Outline each blood parasite and name the species.
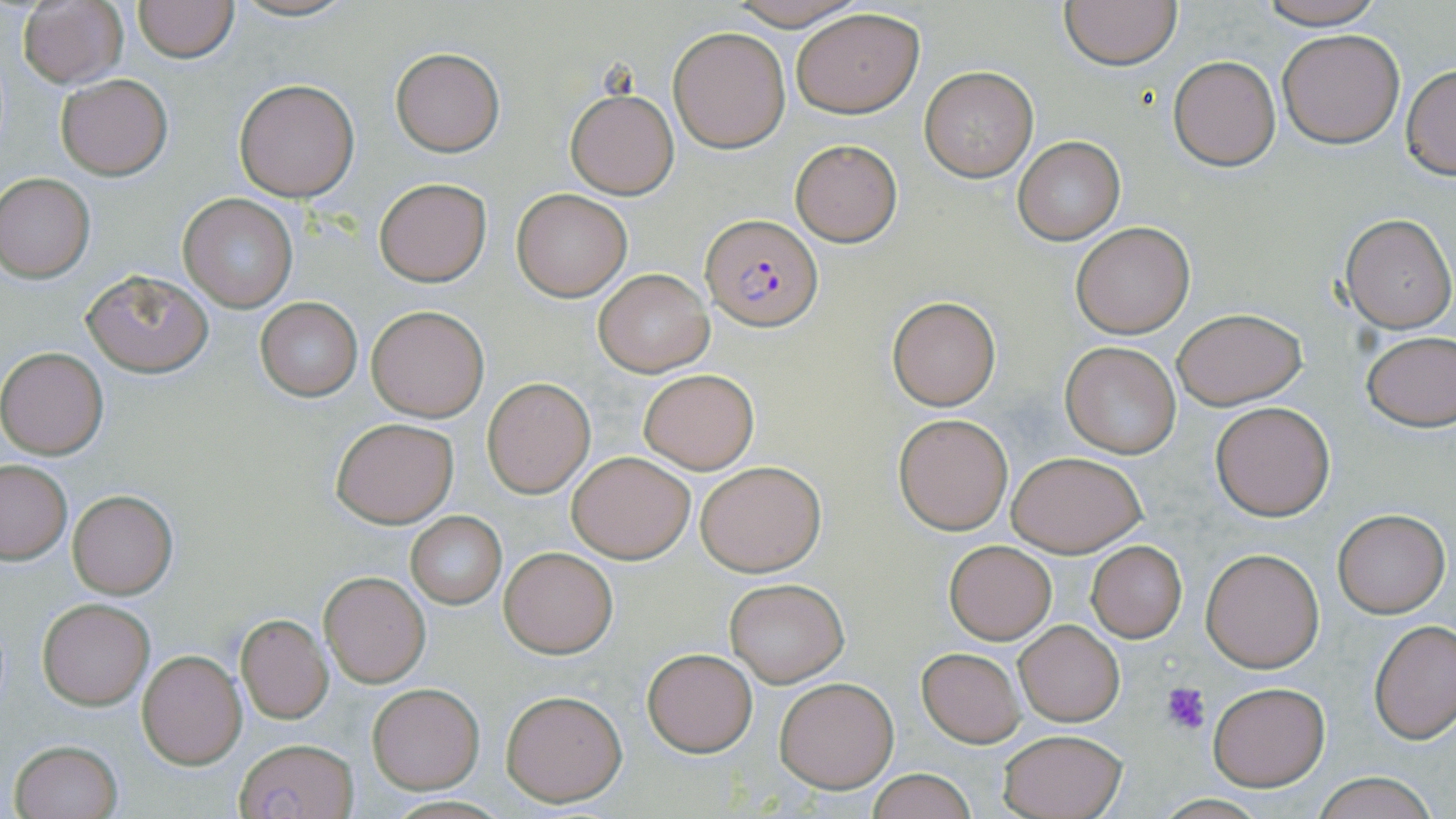

Approximate bounding boxes as [x1, y1, x2, y2] in pixels.
Plasmodium falciparum-infected red blood cells: [702, 214, 824, 333].
No Plasmodium ovale, Plasmodium malariae, Plasmodium vivax, Babesia divergens, or Trypanosoma brucei observed.

Platelet locations: [1162, 681, 1211, 734]. Uninfected red blood cell locations: [133, 0, 239, 62], [227, 0, 357, 22], [723, 0, 873, 29], [1253, 0, 1389, 29], [18, 1, 127, 88], [1060, 1, 1182, 70], [792, 7, 925, 119], [668, 25, 790, 152], [1277, 27, 1406, 148], [390, 47, 504, 155], [1168, 56, 1280, 170], [1401, 63, 1456, 179], [920, 65, 1038, 182], [55, 72, 174, 181], [232, 79, 360, 202], [565, 89, 679, 198], [1013, 137, 1125, 244], [789, 139, 902, 246], [0, 174, 95, 280], [374, 178, 492, 286], [512, 189, 633, 301], [179, 194, 299, 311], [1338, 212, 1455, 332], [1070, 221, 1195, 338], [593, 269, 712, 377], [82, 270, 212, 377], [255, 296, 363, 400], [887, 297, 1000, 410], [367, 306, 489, 420], [1171, 308, 1306, 409], [1361, 329, 1456, 431], [1060, 340, 1183, 459], [0, 348, 108, 459], [637, 367, 759, 473], [483, 378, 594, 497], [1211, 402, 1335, 521], [894, 413, 1013, 535], [330, 416, 459, 528], [566, 450, 694, 563], [1007, 451, 1148, 557], [695, 459, 826, 576], [0, 460, 72, 563], [66, 489, 177, 597], [1332, 506, 1451, 618], [405, 512, 507, 609], [943, 540, 1056, 643], [1086, 541, 1187, 642], [498, 545, 618, 658], [1201, 546, 1326, 671], [320, 571, 430, 686], [724, 577, 849, 686], [39, 599, 153, 710], [235, 615, 333, 723], [1370, 618, 1455, 742], [1014, 620, 1124, 727], [641, 647, 757, 757], [916, 647, 1025, 747], [137, 648, 247, 769], [775, 676, 900, 792], [1207, 682, 1329, 789], [367, 684, 483, 792], [500, 689, 627, 806], [996, 727, 1129, 819], [233, 737, 362, 819], [10, 740, 123, 819], [867, 768, 977, 819], [1309, 774, 1440, 819]. Slide-level diagnosis: Plasmodium falciparum. Image is 1456×819 pixels. Optical microscopy. Single field of view. Thin blood film. May-Grünwald-Giemsa-stained preparation. 1000x magnification.